Identify the parasite.
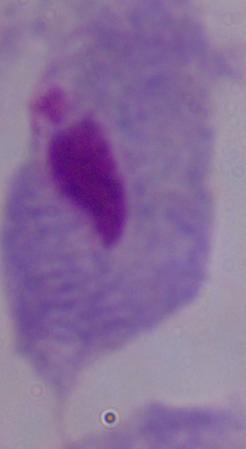

This is a trichomonad.

modality: micrograph
magnification: 1000x